Assess the morphology of the erythrocytes.
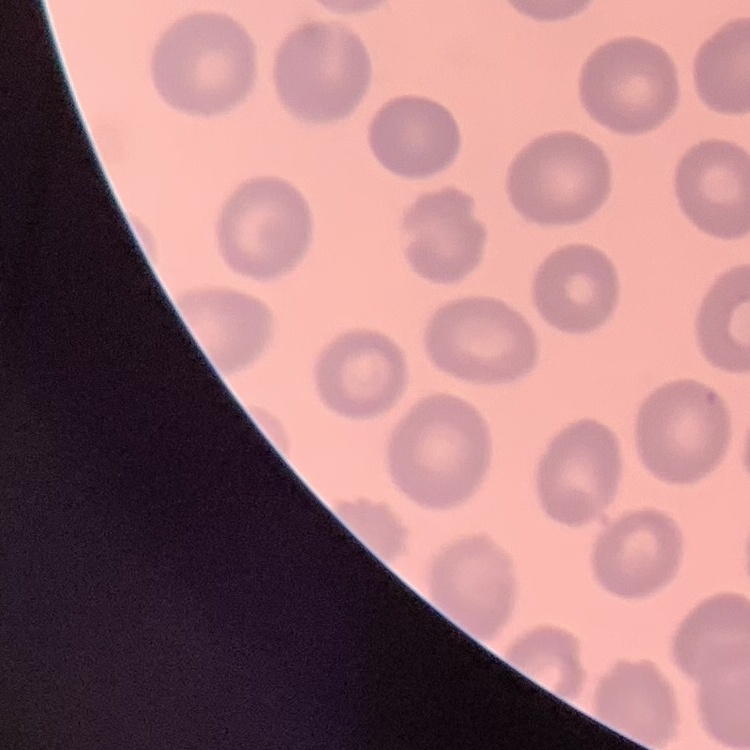

No rouleaux formation.

Thin peripheral smear. One tile cut from a larger photomicrograph. Stained with either Field's or Giemsa.